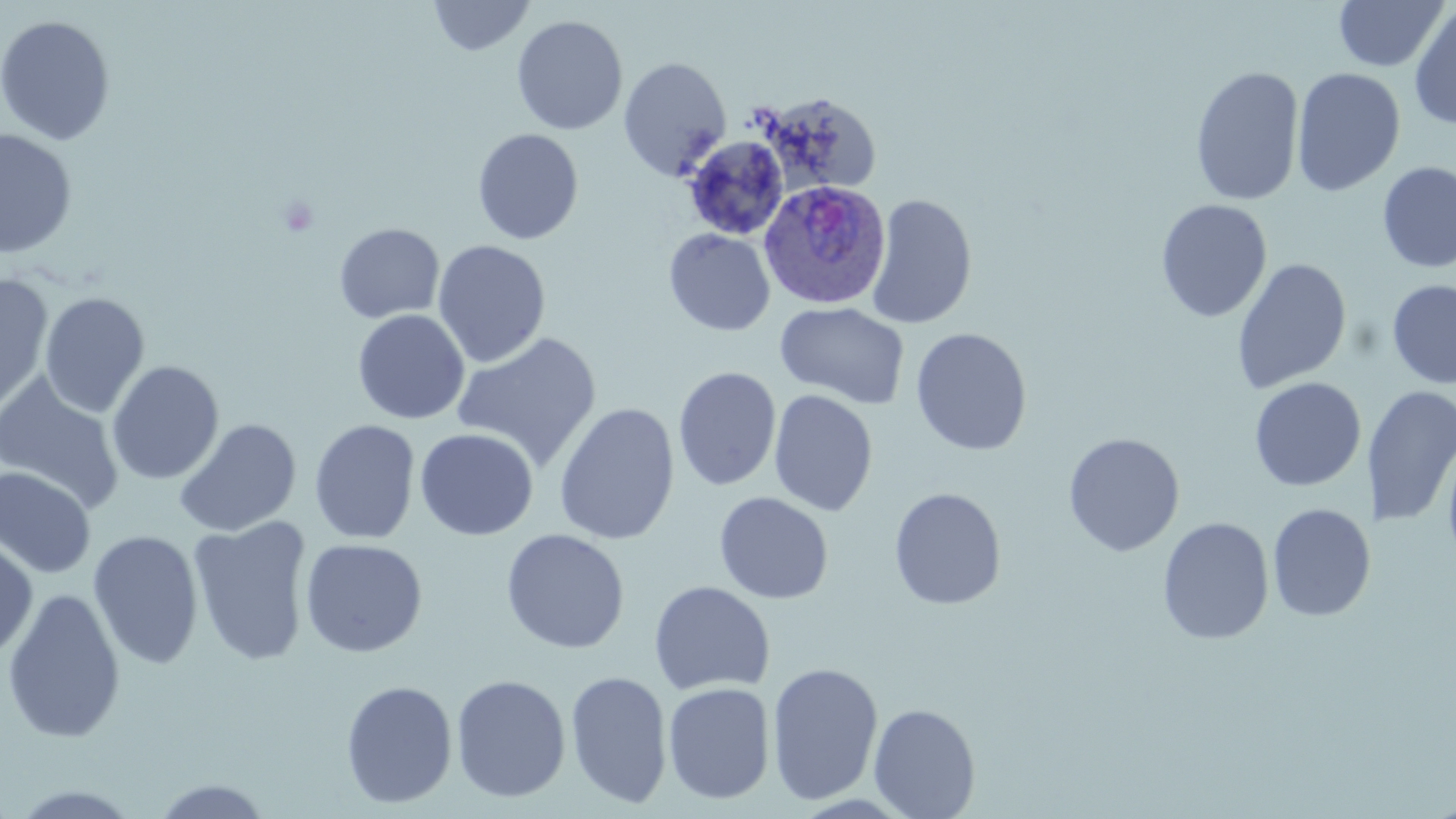
Approximate bounding boxes as (x1,y1)-(x2,y2) corner pairs in pixels. Uninfected red blood cell locations: (428,0)-(535,57), (1332,0)-(1450,72), (1408,4)-(1456,130), (0,14)-(116,146), (511,15)-(628,135), (618,56)-(732,180), (1190,65)-(1305,206), (1292,67)-(1406,197), (753,90)-(883,198), (472,128)-(584,245), (0,129)-(78,259), (681,135)-(789,240), (1376,161)-(1456,273), (865,193)-(978,330), (1155,199)-(1272,323), (333,223)-(445,323), (663,228)-(775,336), (432,239)-(551,368), (1231,258)-(1352,394), (0,273)-(55,414), (1387,280)-(1456,389), (40,292)-(150,418), (774,301)-(910,410), (54,304)-(193,469), (352,309)-(470,424), (910,327)-(1032,456), (451,332)-(603,474), (106,361)-(224,485), (673,366)-(781,491), (0,374)-(124,514), (1249,377)-(1366,491), (1364,385)-(1456,528), (768,389)-(878,516), (553,402)-(680,545), (174,418)-(301,538), (309,419)-(421,544), (415,428)-(539,540), (1062,433)-(1185,557), (1441,437)-(1456,572), (0,466)-(96,579), (888,487)-(1007,610), (713,491)-(834,604), (1267,503)-(1375,622), (188,516)-(313,666), (1157,517)-(1274,645), (500,528)-(630,654), (88,529)-(204,669), (0,537)-(38,663), (300,538)-(428,658), (648,580)-(775,697), (2,587)-(126,744), (766,661)-(884,805), (565,670)-(672,809), (450,674)-(571,803), (339,680)-(458,809), (661,681)-(775,805), (868,703)-(981,819), (148,778)-(275,817). Plasmodium ovale-infected red blood cell locations: (758,180)-(891,310). Slide-level diagnosis: Plasmodium ovale. Image is 1456×819 pixels. Optical microscopy. 1000x magnification. Thin blood smear. Single field of view. May-Grünwald-Giemsa-stained preparation.